Locate every parasitized red blood cell.
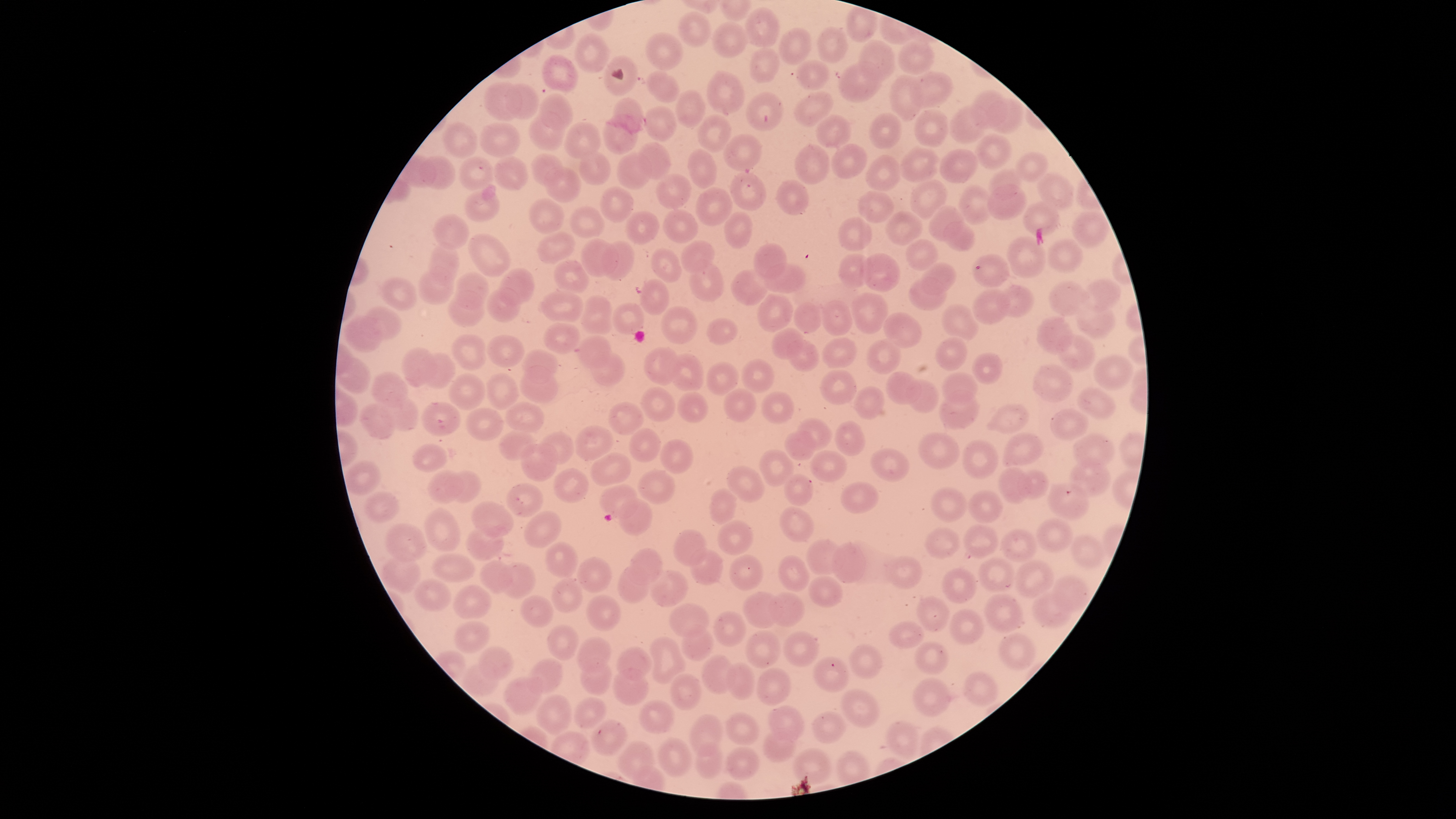
No parasitized red blood cells identified.

Approximate bounding boxes as (left, top, right, bottom) in pixels.
Summary:
  - Uninfected red blood cells: (846, 5, 878, 43), (746, 8, 780, 48), (678, 11, 711, 48), (711, 22, 748, 58), (817, 27, 849, 62), (778, 28, 812, 66), (645, 32, 683, 70), (574, 33, 610, 74), (897, 39, 935, 75), (858, 40, 895, 81), (749, 47, 780, 84), (542, 55, 579, 91), (605, 56, 638, 96), (794, 59, 831, 89), (837, 62, 882, 101), (646, 70, 680, 103), (706, 70, 744, 114), (910, 70, 954, 108), (889, 76, 923, 121), (483, 81, 522, 121), (505, 84, 538, 118), (674, 89, 705, 130), (793, 90, 834, 128), (971, 90, 1009, 130), (539, 92, 574, 130), (745, 92, 785, 131), (989, 97, 1026, 134), (613, 98, 643, 134), (643, 106, 677, 141), (949, 106, 990, 145), (914, 108, 948, 149), (528, 110, 564, 151), (869, 112, 902, 149), (602, 113, 640, 156), (816, 113, 851, 149), (698, 115, 732, 152), (443, 122, 479, 157), (480, 122, 521, 158), (564, 122, 601, 159), (724, 133, 761, 171), (975, 135, 1013, 170), (636, 142, 671, 179), (830, 143, 868, 179), (794, 144, 830, 185), (899, 146, 941, 183), (687, 149, 718, 189), (939, 149, 979, 183), (577, 151, 610, 185), (1015, 151, 1049, 183), (616, 152, 652, 190), (531, 154, 564, 187), (418, 155, 456, 191), (864, 155, 900, 192), (492, 156, 530, 192), (459, 157, 495, 191), (544, 166, 582, 203), (988, 168, 1023, 202), (728, 171, 766, 211), (1036, 173, 1076, 211), (656, 174, 690, 209), (776, 178, 809, 216), (910, 179, 950, 221), (958, 183, 995, 224), (987, 183, 1027, 221), (598, 187, 634, 223), (695, 187, 733, 226), (463, 189, 500, 223), (857, 190, 894, 224), (528, 199, 563, 233), (1020, 201, 1059, 237), (928, 205, 964, 242), (569, 207, 604, 239), (663, 207, 700, 245), (885, 210, 923, 246), (1071, 210, 1111, 248), (624, 211, 660, 245), (724, 212, 753, 249), (432, 214, 469, 250), (838, 216, 872, 251), (943, 222, 976, 252), (537, 231, 575, 264), (468, 233, 511, 277), (1007, 236, 1046, 280), (581, 239, 619, 276), (905, 239, 939, 271), (1047, 239, 1082, 275), (600, 240, 635, 281), (680, 241, 716, 273), (428, 242, 459, 284), (753, 243, 787, 281), (650, 248, 683, 283), (837, 253, 875, 288), (859, 253, 901, 292), (972, 254, 1009, 289), (553, 259, 590, 293), (688, 260, 724, 302), (921, 261, 957, 295), (765, 262, 806, 293), (497, 267, 535, 307), (731, 269, 768, 308), (417, 270, 455, 303), (456, 272, 489, 304), (378, 276, 418, 313), (907, 276, 948, 311), (639, 278, 670, 315), (1082, 279, 1121, 313), (1048, 282, 1091, 318), (995, 283, 1035, 319), (485, 286, 521, 323), (970, 289, 1011, 326), (449, 290, 485, 326), (543, 291, 583, 322), (757, 293, 795, 333), (852, 294, 887, 334), (581, 296, 612, 334), (821, 301, 852, 337), (793, 302, 823, 335), (941, 303, 980, 343), (612, 304, 645, 336), (1076, 304, 1114, 338), (661, 306, 697, 344), (367, 308, 402, 340), (882, 313, 922, 348), (344, 317, 383, 352), (1036, 317, 1072, 354), (706, 318, 738, 344), (543, 322, 581, 354), (772, 327, 803, 359), (452, 334, 485, 371), (1055, 334, 1096, 372), (485, 335, 525, 367), (575, 335, 611, 367), (936, 336, 967, 372), (822, 337, 856, 369), (786, 338, 818, 372), (866, 338, 902, 374), (643, 347, 679, 385), (400, 348, 438, 387), (523, 349, 558, 385), (419, 352, 456, 389), (590, 352, 627, 386), (668, 353, 705, 390), (973, 353, 1003, 384), (1093, 356, 1133, 391), (337, 359, 373, 395), (740, 360, 775, 394), (706, 362, 739, 395), (1031, 365, 1075, 402), (522, 366, 559, 403), (819, 370, 856, 404), (941, 371, 978, 404), (886, 372, 921, 405), (371, 373, 409, 407), (449, 373, 487, 410), (485, 373, 520, 409), (905, 380, 940, 413), (640, 386, 677, 422), (854, 386, 886, 421), (723, 387, 758, 422), (1077, 387, 1117, 419), (677, 390, 708, 423), (938, 390, 980, 429), (378, 392, 419, 431), (761, 392, 794, 423), (607, 400, 644, 436), (421, 401, 461, 435), (358, 403, 394, 440), (504, 403, 544, 432), (985, 404, 1029, 433), (465, 407, 504, 441), (1050, 408, 1089, 441), (796, 418, 831, 447), (834, 420, 864, 457), (575, 425, 614, 459), (628, 428, 661, 462), (784, 430, 817, 460), (497, 431, 537, 462), (918, 432, 961, 470), (1002, 432, 1044, 468), (537, 433, 574, 466), (1072, 433, 1115, 468), (961, 439, 998, 478), (661, 441, 694, 474), (519, 444, 558, 481), (412, 446, 448, 473), (869, 448, 910, 481), (758, 450, 795, 485), (810, 450, 847, 483), (591, 452, 631, 485), (1071, 459, 1111, 498), (345, 461, 382, 495), (726, 466, 765, 502), (553, 468, 590, 503), (998, 468, 1032, 504), (1017, 468, 1049, 501), (447, 469, 482, 504), (638, 469, 676, 503), (428, 470, 464, 503), (784, 474, 816, 505), (1048, 482, 1089, 520), (506, 483, 543, 518), (600, 484, 637, 517), (840, 484, 878, 514), (930, 487, 968, 523), (708, 488, 737, 524), (968, 490, 1004, 525), (364, 492, 399, 521), (618, 498, 652, 536), (472, 502, 513, 538), (781, 506, 814, 542), (422, 507, 461, 554), (526, 511, 560, 548), (1036, 518, 1073, 553), (717, 521, 753, 555), (386, 525, 427, 562), (466, 525, 506, 562), (962, 525, 998, 559), (924, 527, 960, 560), (1001, 529, 1037, 563), (673, 530, 707, 566), (1070, 535, 1106, 569), (804, 538, 846, 576), (546, 540, 579, 578), (832, 544, 866, 583), (689, 548, 724, 584), (627, 549, 663, 587), (431, 553, 475, 583), (728, 555, 765, 591), (886, 555, 923, 589), (381, 556, 421, 592), (577, 556, 611, 592), (778, 556, 810, 593), (977, 559, 1014, 593), (479, 561, 512, 594), (1014, 561, 1054, 598), (500, 562, 537, 598), (618, 565, 653, 605), (941, 568, 977, 604), (648, 570, 687, 607), (1051, 574, 1090, 612), (810, 576, 843, 608), (553, 578, 582, 612), (414, 580, 451, 610), (452, 584, 492, 620), (744, 591, 783, 628), (983, 592, 1024, 632), (586, 593, 620, 631), (768, 593, 804, 626), (1032, 593, 1071, 628), (519, 595, 554, 629), (917, 596, 951, 634), (668, 605, 709, 639), (948, 610, 985, 645), (712, 611, 746, 647), (454, 621, 490, 653), (888, 621, 924, 648), (547, 626, 578, 660), (679, 629, 714, 662), (744, 630, 782, 667), (782, 632, 819, 667), (996, 632, 1036, 670), (576, 636, 611, 673), (650, 636, 686, 684), (915, 641, 949, 674), (848, 644, 883, 679), (478, 647, 514, 682), (618, 648, 651, 680), (702, 655, 736, 694), (812, 656, 849, 692), (526, 658, 563, 692), (581, 658, 611, 695), (728, 663, 756, 700), (463, 665, 498, 697), (757, 667, 791, 706), (613, 669, 649, 705), (962, 672, 998, 708), (670, 673, 702, 711), (504, 677, 543, 714), (913, 678, 950, 716), (839, 689, 880, 727), (537, 695, 572, 734), (573, 698, 607, 729), (639, 700, 675, 734), (769, 704, 804, 740), (814, 711, 846, 745), (726, 712, 759, 745), (689, 714, 723, 756), (883, 719, 920, 758), (591, 721, 628, 756), (763, 729, 797, 762), (658, 737, 693, 776), (618, 740, 655, 780), (694, 744, 724, 779), (726, 746, 760, 780), (793, 747, 832, 785)
  - Image size: 1456×819 pixels
  - Stain: Giemsa
  - Capture: smartphone photograph through the microscope eyepiece
  - Preparation: thin blood film
  - Visible region: circular
  - Field of view: single